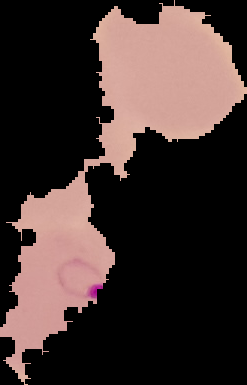

result: Plasmodium parasites identified
preparation: thin blood film
image_size: 247×385 pixels
image_type: segmented cell region on a black background